Identify the cell.
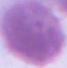

An erythrocyte.

Summary:
  - Magnification: 1000x
  - Modality: micrograph